Classify this cell by malaria status.
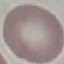

Uninfected.

preparation = thin blood film
stain = Giemsa
image type = cell patch, automatically extracted from a larger field of view and resized to 64 × 64 pixels
capture = smartphone camera at the microscope eyepiece